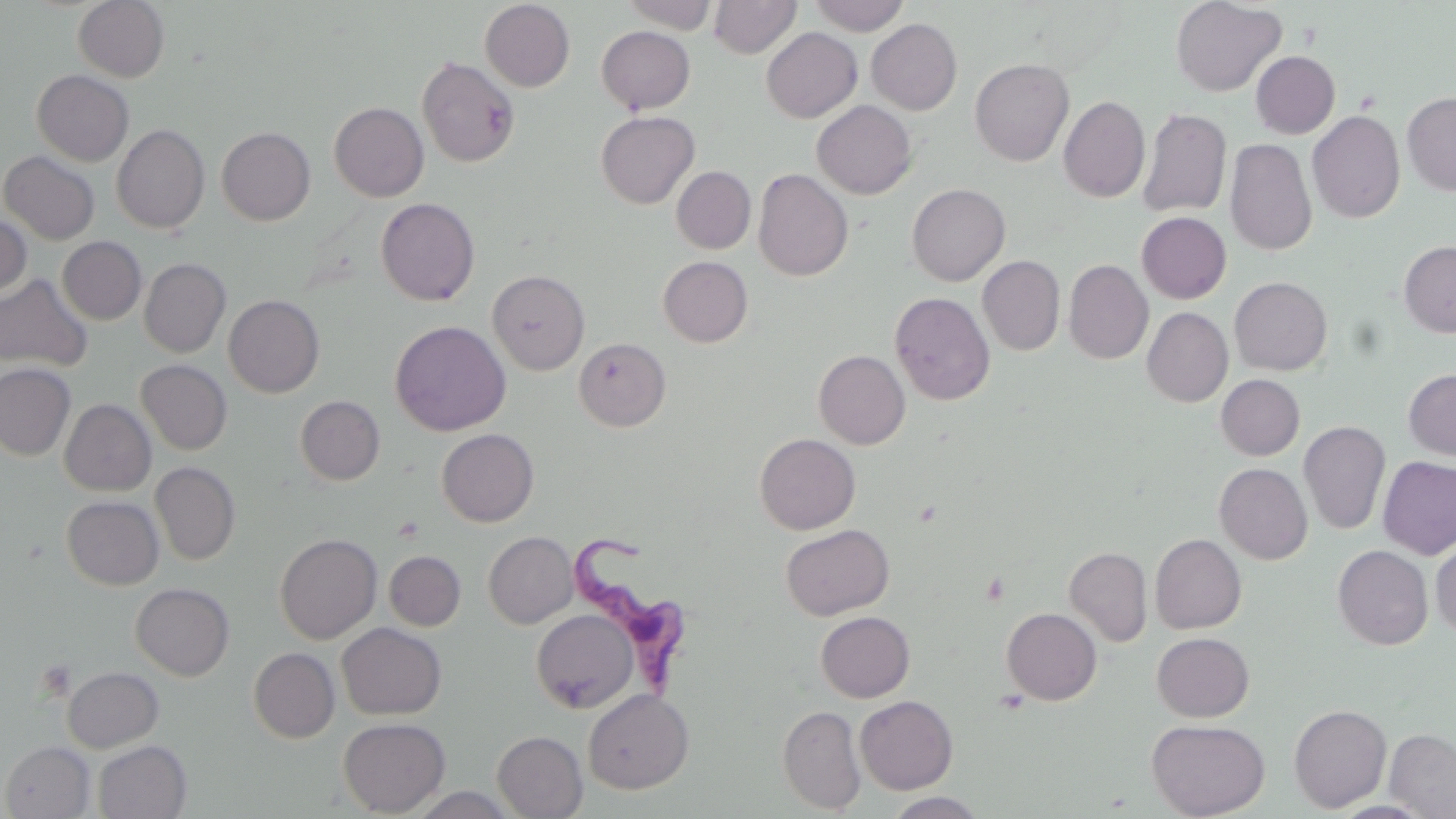

Summary:
  - Coordinate format: approximate bounding boxes as (x1, y1, x2, y2) in pixels
  - Platelet locations: (983, 572, 1009, 605)
  - Uninfected red blood cell locations: (73, 0, 169, 82), (620, 0, 719, 33), (710, 0, 801, 58), (808, 0, 911, 35), (1170, 0, 1286, 96), (480, 1, 575, 91), (867, 19, 962, 114), (596, 26, 694, 114), (761, 27, 862, 122), (1251, 51, 1340, 138), (417, 56, 520, 168), (970, 58, 1074, 166), (32, 70, 134, 166), (1402, 90, 1456, 196), (1058, 96, 1150, 202), (812, 100, 917, 199), (329, 102, 429, 202), (1137, 107, 1231, 218), (1307, 110, 1405, 223), (596, 111, 699, 209), (112, 124, 210, 233), (216, 127, 316, 225), (1225, 138, 1317, 255), (1, 151, 100, 244), (672, 166, 756, 253), (753, 169, 853, 281), (907, 183, 1010, 285), (376, 198, 480, 305), (1137, 212, 1231, 303), (0, 213, 31, 300), (58, 237, 146, 324), (1399, 240, 1456, 337), (977, 255, 1065, 355), (658, 256, 753, 347), (139, 258, 230, 357), (1063, 259, 1153, 364), (488, 270, 590, 374), (0, 273, 93, 373), (1229, 277, 1332, 375), (890, 291, 995, 405), (224, 294, 324, 397), (1142, 307, 1233, 407), (390, 320, 511, 436), (574, 337, 671, 431), (813, 350, 910, 449), (136, 360, 232, 455), (0, 363, 75, 460), (1403, 369, 1456, 461), (1216, 374, 1305, 460), (295, 395, 385, 485), (60, 400, 156, 496), (1299, 421, 1390, 535), (436, 428, 539, 526), (754, 433, 860, 534), (1378, 456, 1456, 559), (150, 463, 240, 565), (1215, 463, 1312, 564), (61, 496, 163, 590), (780, 524, 894, 620), (484, 531, 578, 628), (274, 534, 382, 643), (1150, 534, 1246, 633), (1431, 539, 1456, 639), (1333, 545, 1433, 650), (1064, 546, 1152, 647), (384, 551, 465, 630), (131, 583, 234, 680), (1001, 607, 1102, 705), (531, 609, 638, 713), (815, 611, 915, 702), (337, 623, 446, 720), (1152, 632, 1254, 721), (248, 648, 340, 743), (62, 666, 163, 753), (582, 688, 694, 794), (855, 695, 958, 794), (1289, 704, 1392, 812), (778, 705, 867, 814), (338, 717, 450, 816), (1146, 718, 1270, 819), (1385, 728, 1456, 818), (492, 731, 587, 818), (93, 740, 191, 819), (0, 741, 95, 818), (883, 792, 989, 818)
  - Trypanosoma brucei locations: (571, 532, 684, 692)
  - Slide-level diagnosis: Trypanosoma brucei
  - Preparation: thin blood film
  - Image size: 1456×819 pixels
  - Magnification: 1000x
  - Field of view: one of a larger specimen
  - Modality: optical microscopy
  - Stain: May-Grünwald-Giemsa